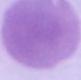

{
  "modality": "micrograph",
  "magnification": "1000x",
  "identification": "red blood cell"
}